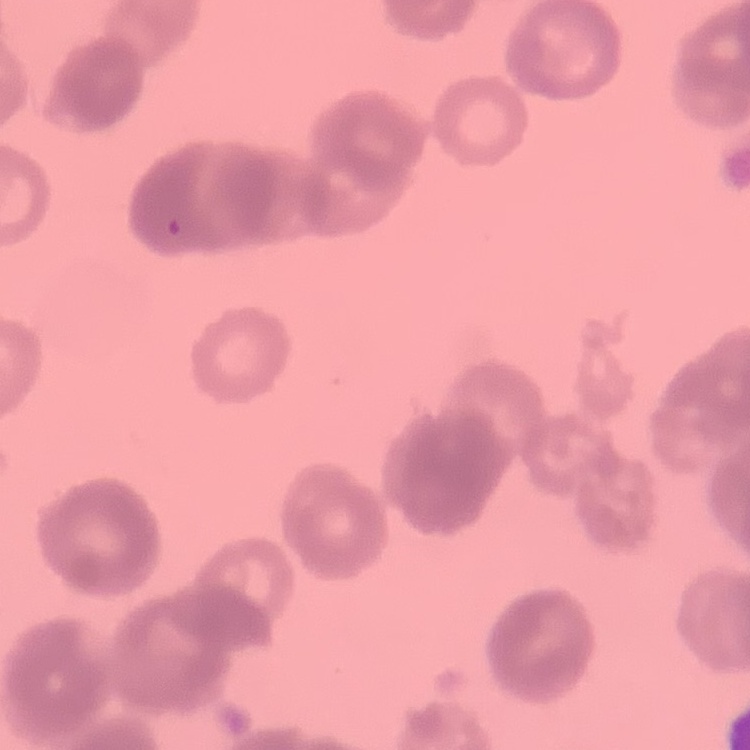

Summary:
  - Red blood cell morphology: rouleaux formation
  - Preparation: thin peripheral smear
  - Stain: Field's or Giemsa
  - Image type: square crop of a larger photomicrograph